Comment on the morphology of the erythrocytes.
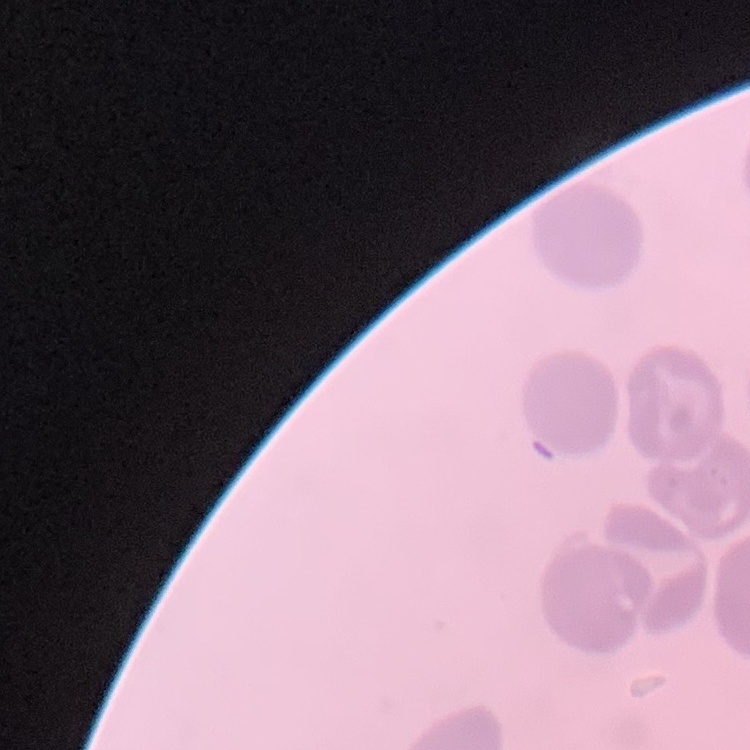

They show no rouleaux formation.

Summary:
  - Preparation: thin peripheral smear
  - Stain: Field's or Giemsa
  - Image type: one tile cut from a larger photomicrograph